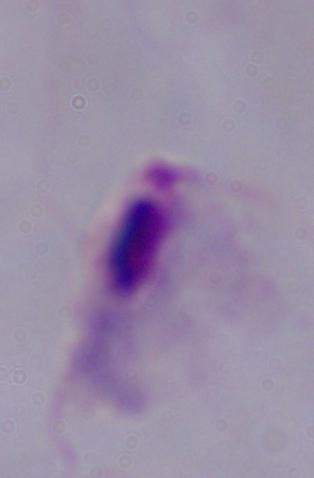

identification = trichomonad
modality = photomicrograph
magnification = 1000x